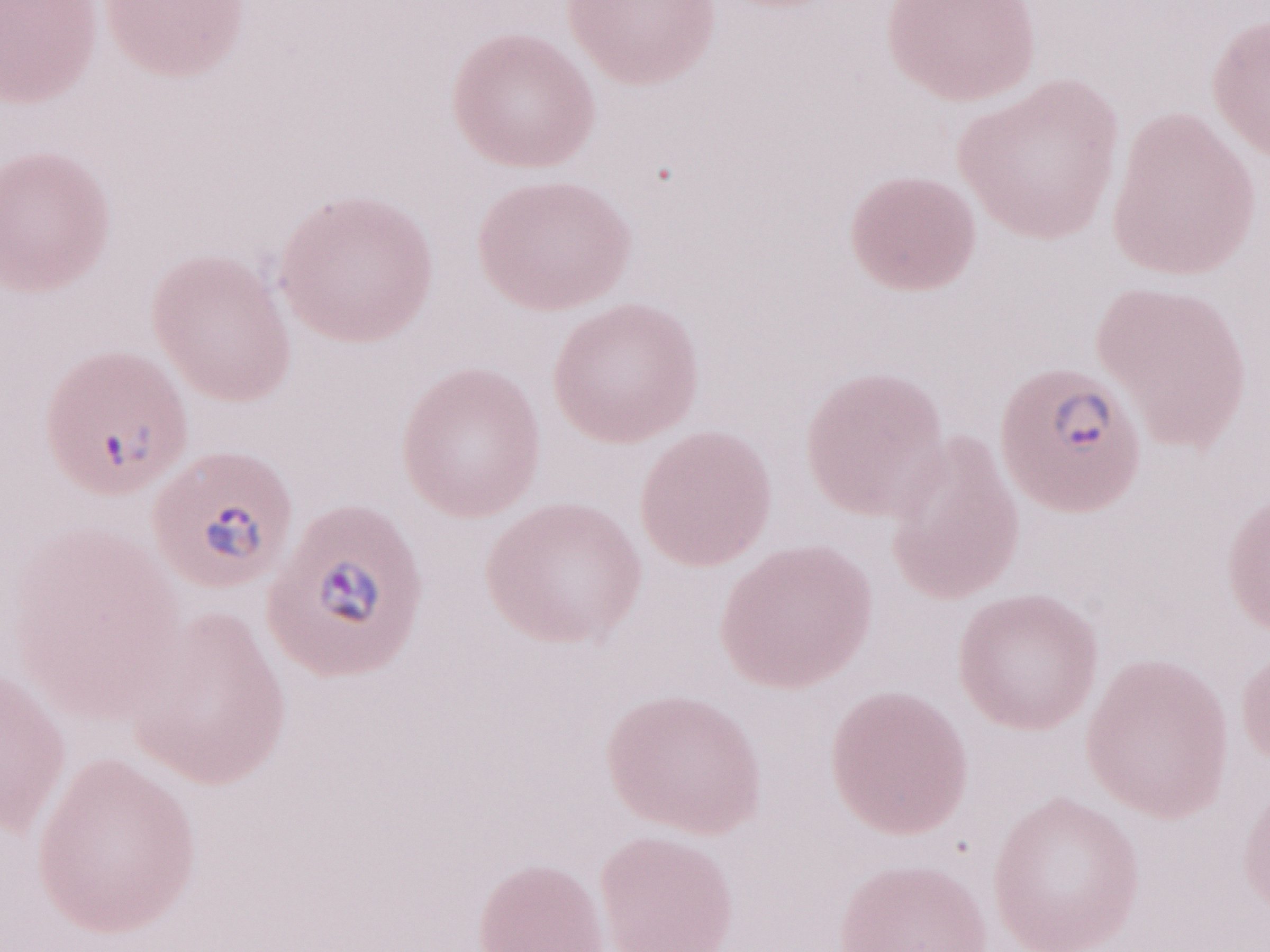
Image is 1270×952 pixels. May-Grünwald-Giemsa (MGG) stain. Magnification: 1,000x. Single field of view. Olympus BX43 microscope and DP73 digital camera. Thin blood film. Malaria diagnosis (patient-level): positive.